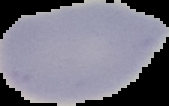

image size = 169×106 pixels
preparation = thin blood film
image type = segmented cell region on a black background
result = no malaria parasites seen